Locate every blood parasite and identify its species.
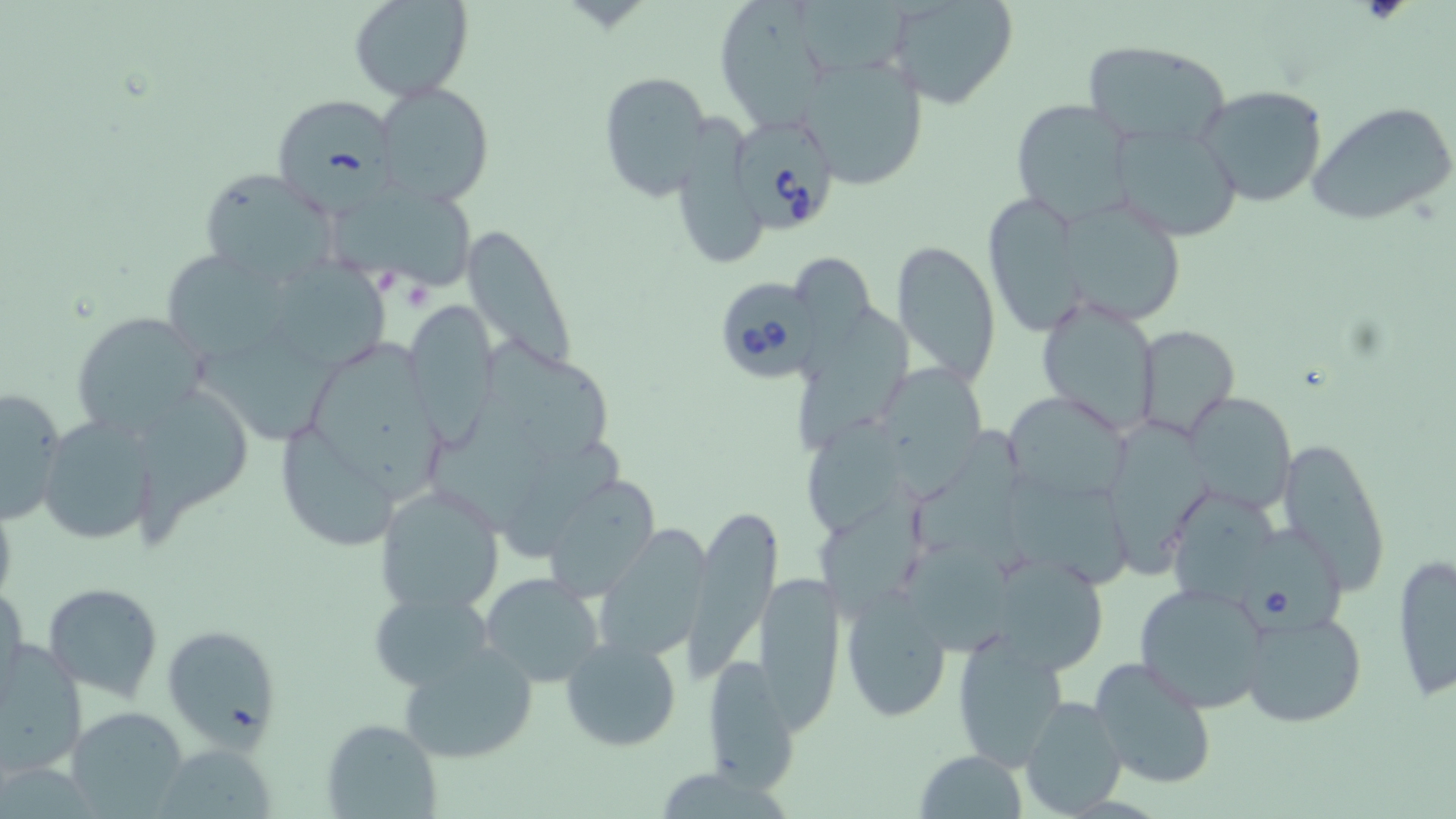
Approximate bounding boxes as [x1, y1, x2, y2] in pixels.
Babesia divergens-infected red blood cells: [734, 123, 838, 230], [717, 280, 825, 382], [1237, 523, 1346, 647].
No Plasmodium falciparum, Plasmodium ovale, Plasmodium malariae, Plasmodium vivax, or Trypanosoma brucei observed.

Uninfected red blood cell locations: [349, 0, 474, 102], [713, 0, 839, 131], [884, 0, 1020, 110], [793, 1, 915, 77], [1081, 41, 1228, 148], [796, 56, 929, 193], [597, 70, 713, 201], [373, 80, 496, 206], [1198, 84, 1329, 208], [271, 95, 398, 213], [1008, 98, 1136, 223], [1308, 101, 1455, 227], [1109, 122, 1245, 239], [198, 168, 342, 290], [332, 187, 483, 296], [986, 194, 1082, 331], [1064, 195, 1194, 321], [461, 221, 580, 375], [890, 238, 1002, 386], [173, 256, 297, 369], [279, 260, 399, 367], [1034, 293, 1162, 433], [405, 300, 501, 440], [796, 307, 911, 452], [70, 309, 211, 439], [1135, 325, 1239, 439], [311, 342, 452, 499], [889, 370, 997, 509], [0, 383, 67, 524], [142, 387, 257, 546], [1186, 390, 1295, 512], [1005, 392, 1133, 504], [38, 413, 162, 547], [1108, 421, 1218, 577], [289, 426, 402, 550], [809, 426, 913, 534], [1275, 433, 1391, 595], [538, 472, 663, 599], [374, 484, 505, 617], [814, 488, 932, 614], [0, 492, 19, 611], [1177, 496, 1285, 619], [685, 501, 779, 678], [595, 532, 709, 665], [1389, 552, 1456, 703], [912, 554, 1026, 652], [992, 554, 1109, 680], [754, 570, 845, 731], [481, 573, 605, 685], [1134, 580, 1271, 712], [0, 581, 27, 697], [42, 581, 164, 700], [840, 587, 953, 724], [366, 588, 494, 690], [1237, 606, 1368, 730], [162, 624, 284, 748], [952, 626, 1070, 769], [560, 636, 682, 752], [395, 640, 540, 766], [0, 641, 88, 777], [701, 652, 798, 793], [1087, 656, 1220, 790], [1018, 695, 1129, 817], [67, 706, 190, 817], [322, 718, 439, 817], [149, 743, 279, 818], [916, 749, 1029, 818]. Slide-level diagnosis: Babesia divergens. Thin blood film. One field of a larger specimen. Image is 1456×819 pixels. Captured at 1000x magnification. May-Grünwald-Giemsa stain. Light microscopy.